State which parasite is depicted.
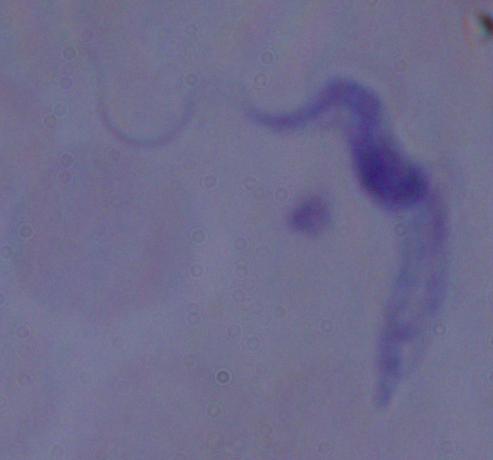

This is a trypanosome.

Micrograph. 1000x magnification.